Give the preparation type.
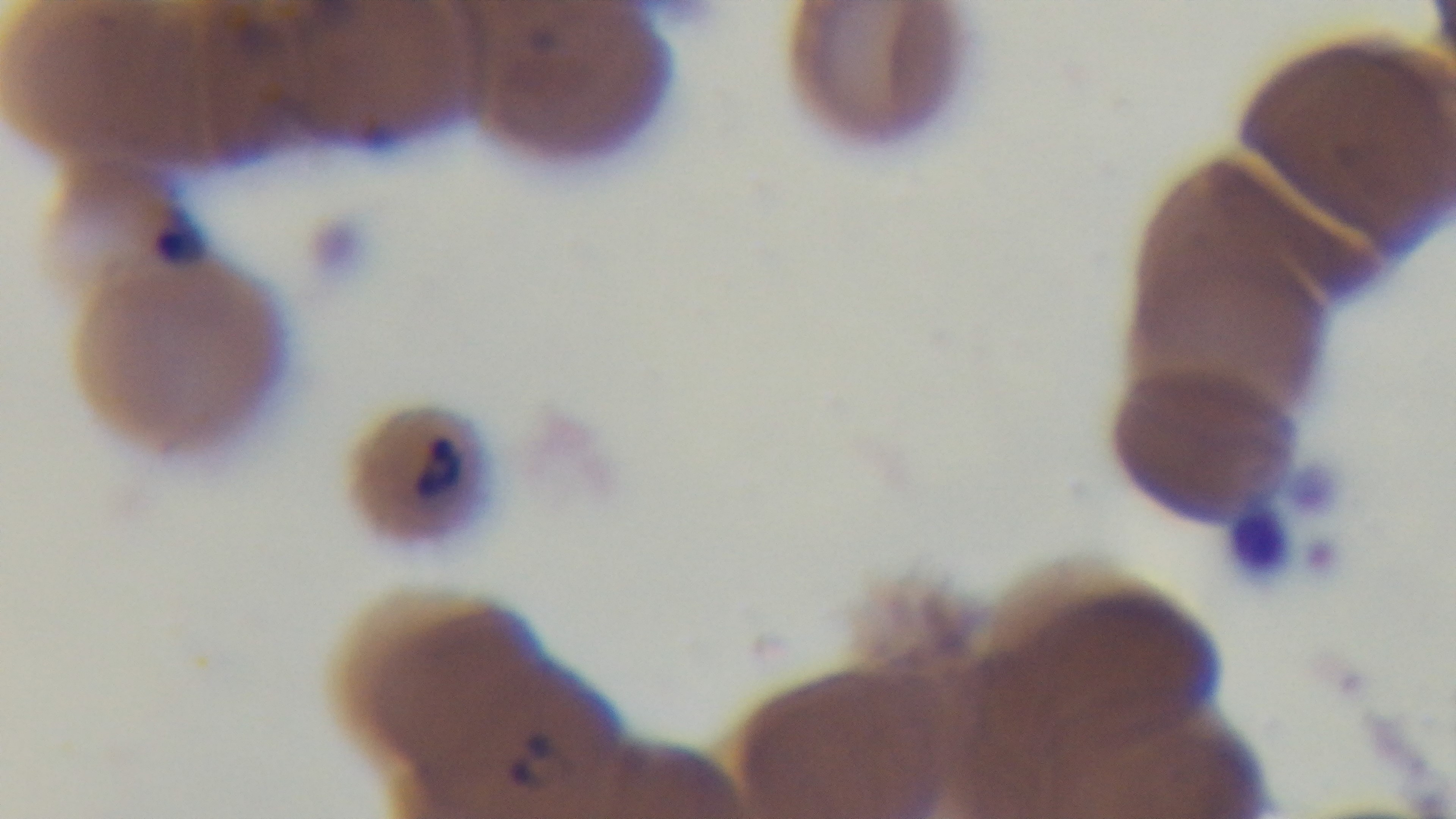
Thin.

Summary:
  - Capture: mounted 4K digital camera
  - Stain: Giemsa
  - Objective: 100x oil immersion
  - Malaria status: infected
  - Field of view: one from the slide
  - Modality: light microscopy